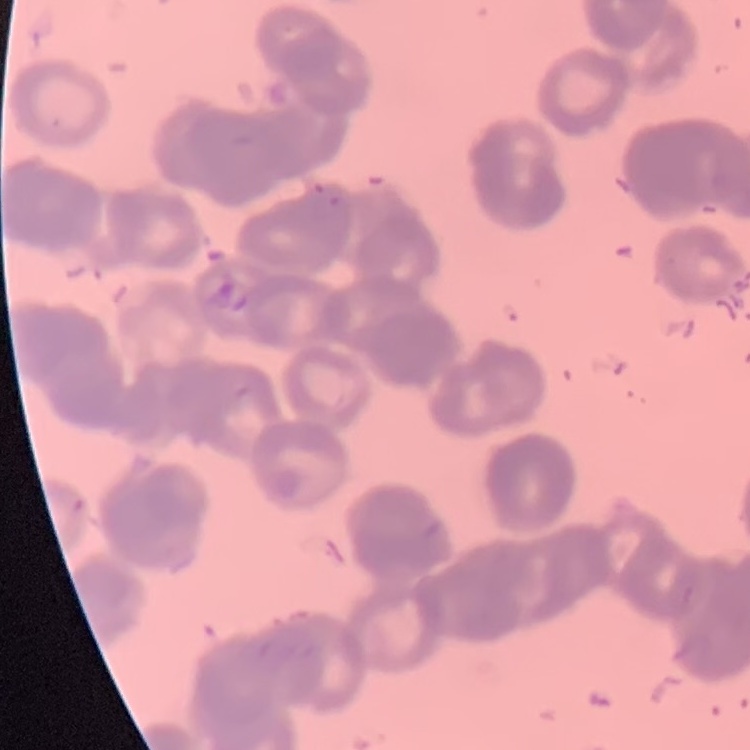

red_blood_cell_morphology: rouleaux formation
preparation: thin peripheral smear
stain: Field's or Giemsa
image_type: square crop of a larger photomicrograph